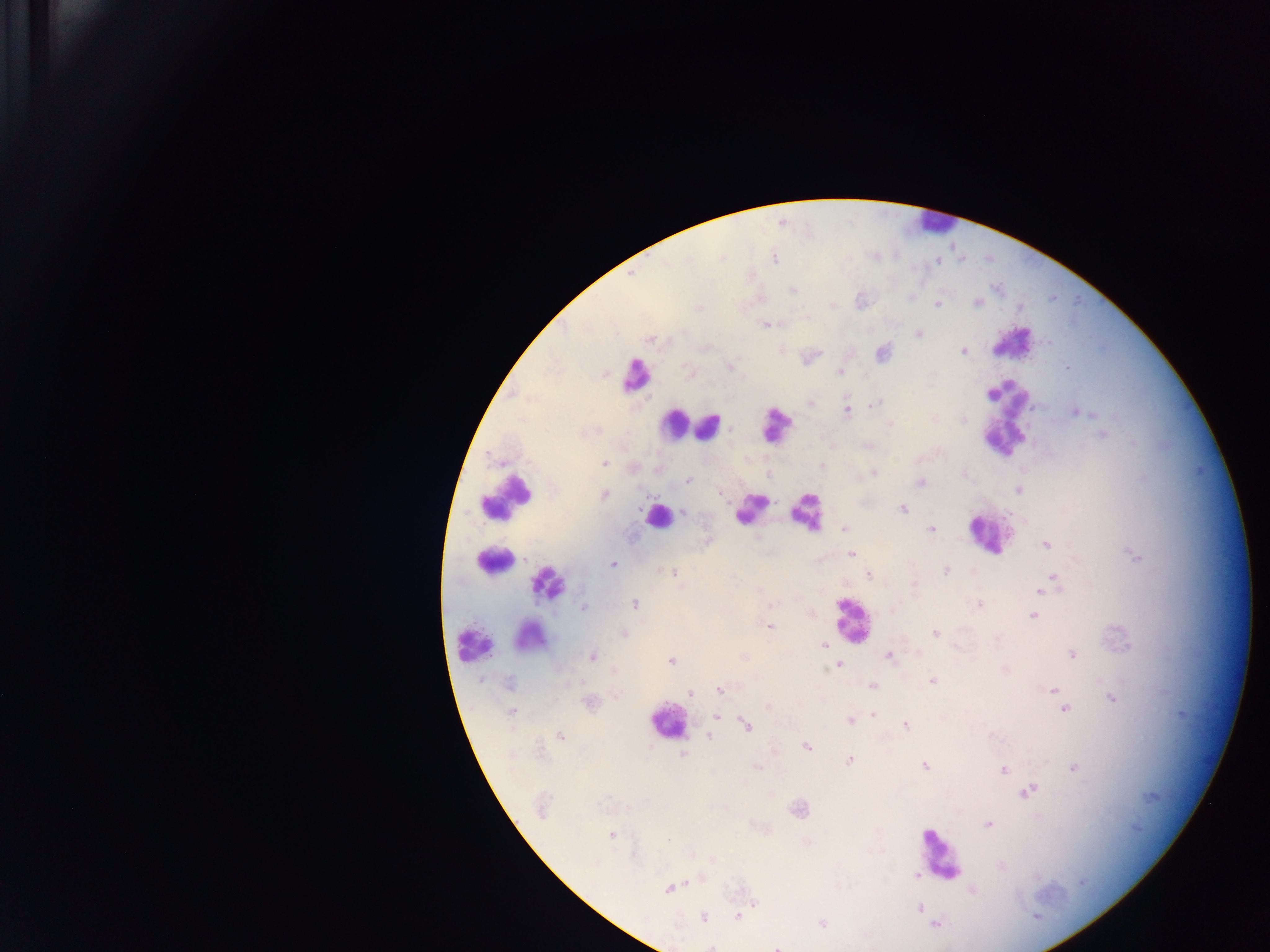
capture = mobile-phone photograph through a microscope
field of view = single
image size = 1270×952 pixels
country = Ghana
leukocyte locations = approximate centers as x y in pixels: 939 225; 1017 347; 636 377; 1008 422; 709 427; 671 429; 772 435; 511 499; 747 511; 657 517; 807 518; 988 533; 501 564; 545 585; 851 619; 533 631; 473 651; 671 724; 941 855
preparation = thick blood film
malaria parasite locations = approximate centers as x y in pixels: 774 258; 938 262; 632 273; 792 291; 977 303; 833 306; 938 306; 1020 307; 766 326; 917 335; 651 339; 963 351; 1066 367; 840 372; 875 404; 847 410; 1076 413; 964 419; 890 425; 596 431; 1103 435; 491 457; 605 464; 874 472; 966 475; 688 480; 922 482; 606 495; 903 510; 684 511; 843 529; 931 529; 1047 544; 851 553; 1138 556; 612 564; 947 570; 674 573; 869 575; 1055 575; 914 585; 1044 587; 1039 592; 771 604; 636 605; 980 605; 584 608; 1034 615; 770 627; 934 633; 997 639; 823 646; 1072 655; 890 656; 592 657; 672 662; 838 665; 1005 668; 933 680; 508 685; 871 685; 719 690; 1053 691; 690 694; 1113 700; 1066 709; 512 713; 873 715; 719 716; 849 720; 747 725; 906 725; 561 735; 710 737; 806 747; 541 750; 684 755; 849 762; 925 766; 1075 768; 1005 770; 1031 791; 542 806; 990 824; 612 836; 670 838; 1000 867; 917 876; 1083 885; 670 888; 974 891; 753 904; 921 908; 737 915; 702 916; 1036 916; 822 923; 937 923; 774 946; 712 947